Outline each Trypanosoma brucei.
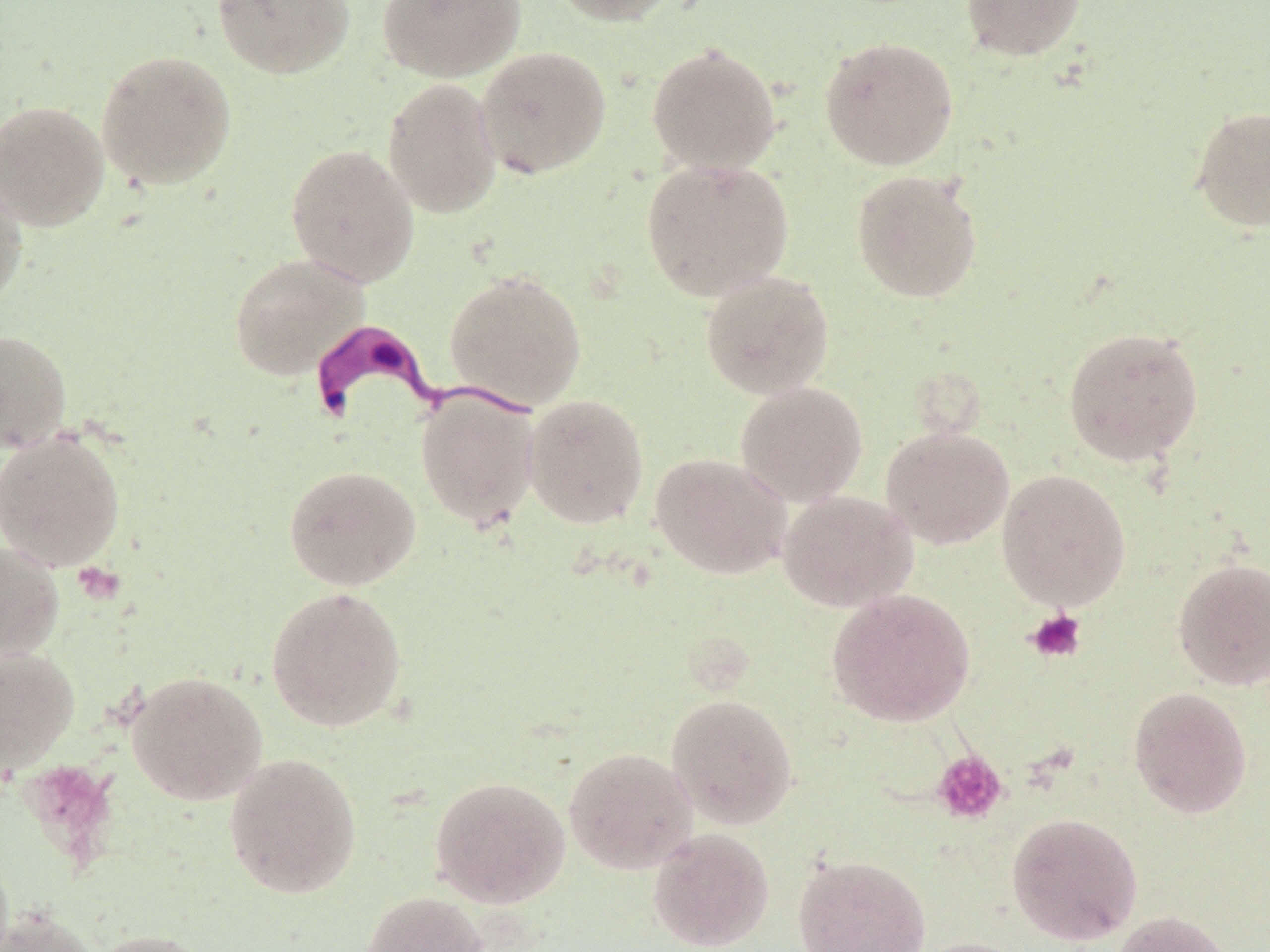
Approximate bounding boxes as (x1,y1)-(x2,y2) corner pairs in pixels.
Trypanosoma brucei: (302,320)-(536,434).

slide-level diagnosis = Trypanosoma brucei
magnification = 1000x
platelet locations = approximate bounding boxes as (x1,y1)-(x2,y2) corner pairs in pixels: (72,561)-(125,606), (1024,608)-(1087,664), (932,750)-(1007,824)
modality = optical microscopy
field of view = one of a larger specimen
preparation = thin blood film
uninfected red blood cell locations = approximate bounding boxes as (x1,y1)-(x2,y2) corner pairs in pixels: (212,0)-(355,79), (377,0)-(525,82), (547,0)-(683,26), (960,0)-(1086,61), (819,36)-(959,170), (646,41)-(782,175), (475,45)-(612,178), (96,49)-(238,190), (383,78)-(503,218), (0,100)-(110,231), (1188,105)-(1270,232), (285,144)-(419,286), (640,158)-(795,302), (851,169)-(984,303), (0,173)-(29,313), (228,252)-(369,381), (444,269)-(588,411), (700,269)-(834,399), (1062,326)-(1204,466), (0,329)-(72,452), (734,381)-(868,507), (415,389)-(542,531), (523,393)-(650,529), (880,426)-(1014,549), (0,430)-(127,572), (650,452)-(792,580), (283,464)-(422,591), (996,469)-(1132,610), (777,490)-(918,612), (0,542)-(64,662), (1172,556)-(1270,690), (265,586)-(408,732), (826,588)-(976,727), (0,647)-(80,773), (126,670)-(268,806), (1128,686)-(1252,818), (665,693)-(799,828), (563,746)-(698,874), (222,751)-(363,900), (429,775)-(571,908), (1006,812)-(1143,945), (647,828)-(775,951), (792,852)-(931,951), (360,890)-(490,952), (0,905)-(101,952), (1109,910)-(1236,952), (84,928)-(219,952), (904,936)-(1032,952)
stain = May-Grünwald-Giemsa
image size = 1270×952 pixels